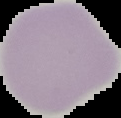

result: negative for Plasmodium parasites
image_type: segmented cell region with the area outside set to black
image_size: 121×118 pixels
preparation: thin blood film